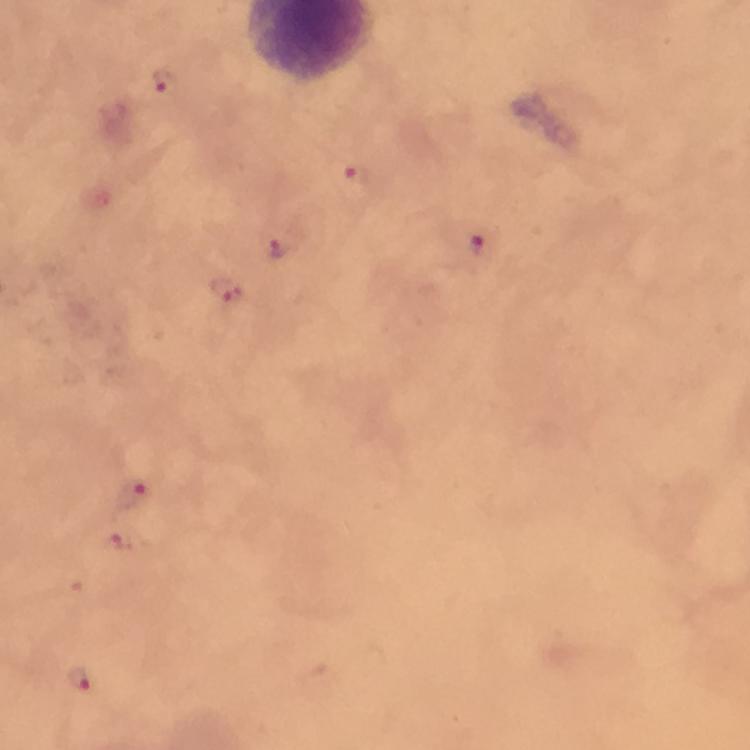

Approximate centers as [x, y] in pixels. Malaria parasite locations: [163, 80], [357, 179], [479, 244], [280, 248], [225, 290], [130, 493], [121, 540], [78, 678]. Thick blood film. Photographed through the microscope with a smartphone camera. Giemsa-stained preparation. Image is 750×750 pixels. Immersion oil applied. At 100x magnification. From a diagnostic examination for malaria. A crop from one field of view.